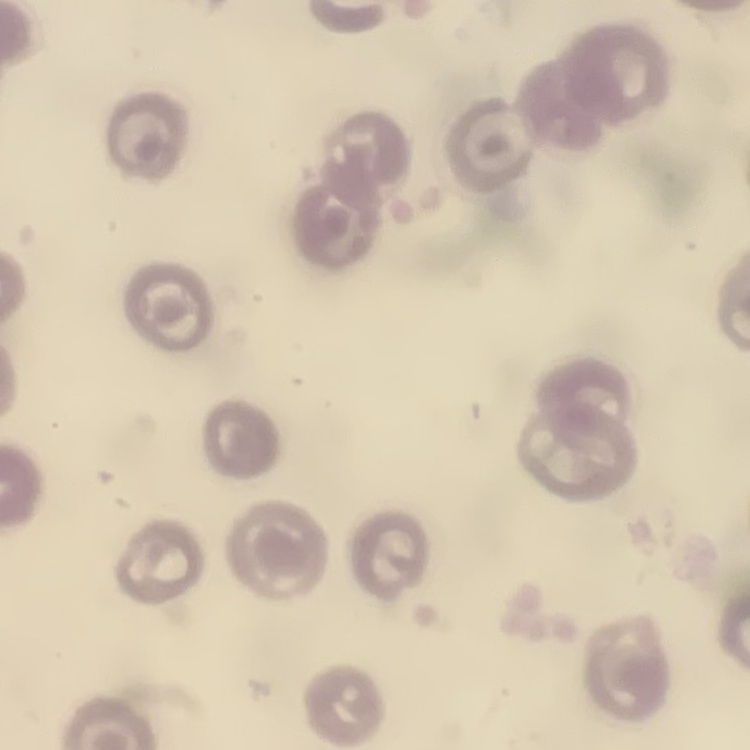
erythrocyte morphology = no rouleaux formation
stain = Field's or Giemsa
preparation = thin blood film
image type = square crop of a larger photomicrograph